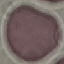 Result: negative for malaria parasites. Giemsa-stained preparation. Automatically extracted cell patch, resized to 64 × 64 pixels. Acquired by smartphone through the microscope eyepiece. Thin blood smear.